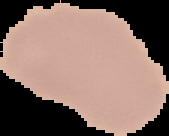

Summary:
  - Image size: 169×136 pixels
  - Preparation: thin blood smear
  - Result: negative for malaria parasites
  - Image type: cell region segmented out of the field of view; surrounding area masked to black